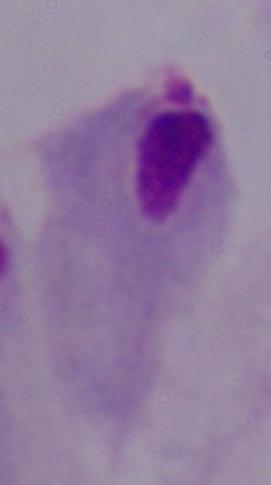

Summary:
  - Magnification: 1000x
  - Modality: micrograph
  - Identification: trichomonad